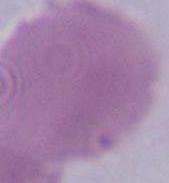

modality = micrograph
magnification = 1000x
identification = red blood cell